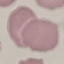

malaria status = uninfected
preparation = thin blood smear
image type = cell patch, automatically extracted from a larger field of view and resized to 64 × 64 pixels
capture = smartphone through the microscope eyepiece
stain = Giemsa